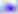 400x magnification. Toxoplasma gondii is shown. Micrograph.